Classify this cell by malaria status.
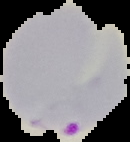
It is parasitized.

From a thin blood smear. Cell region segmented out of the field of view; the surrounding area is masked to black. Image is 130×142 pixels.